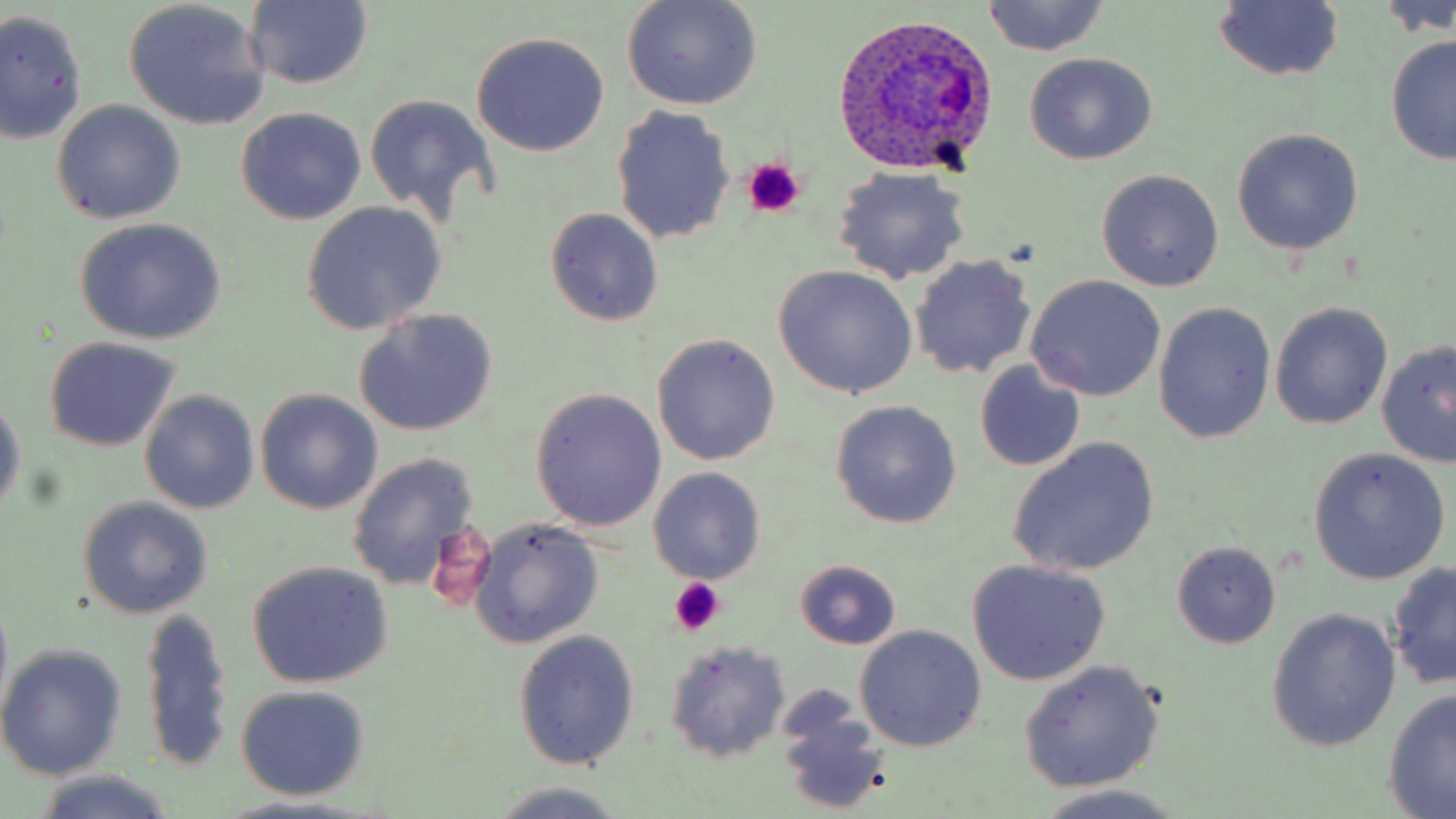 Approximate bounding boxes as named x1/y1/x2/y2 corners in pixels. Plasmodium ovale-infected red blood cell locations: (x1=831, y1=13, x2=998, y2=174). Platelet locations: (x1=742, y1=159, x2=804, y2=219), (x1=668, y1=579, x2=726, y2=636). Uninfected red blood cell locations: (x1=620, y1=0, x2=763, y2=110), (x1=1382, y1=0, x2=1455, y2=38), (x1=246, y1=1, x2=373, y2=89), (x1=1210, y1=1, x2=1345, y2=83), (x1=123, y1=2, x2=270, y2=129), (x1=983, y1=2, x2=1111, y2=56), (x1=1, y1=11, x2=88, y2=145), (x1=473, y1=31, x2=610, y2=156), (x1=1384, y1=35, x2=1456, y2=166), (x1=1024, y1=52, x2=1157, y2=166), (x1=364, y1=93, x2=498, y2=223), (x1=52, y1=101, x2=184, y2=223), (x1=236, y1=107, x2=367, y2=225), (x1=611, y1=107, x2=735, y2=243), (x1=1231, y1=127, x2=1364, y2=255), (x1=832, y1=166, x2=972, y2=285), (x1=1096, y1=169, x2=1224, y2=291), (x1=300, y1=202, x2=447, y2=335), (x1=545, y1=207, x2=665, y2=327), (x1=75, y1=218, x2=226, y2=344), (x1=910, y1=253, x2=1036, y2=380), (x1=773, y1=265, x2=918, y2=399), (x1=1027, y1=275, x2=1167, y2=400), (x1=1153, y1=302, x2=1276, y2=443), (x1=1269, y1=302, x2=1392, y2=430), (x1=353, y1=309, x2=498, y2=436), (x1=652, y1=334, x2=781, y2=466), (x1=45, y1=338, x2=180, y2=452), (x1=1377, y1=340, x2=1456, y2=468), (x1=975, y1=360, x2=1085, y2=473), (x1=255, y1=388, x2=383, y2=514), (x1=529, y1=388, x2=667, y2=532), (x1=140, y1=390, x2=259, y2=513), (x1=0, y1=391, x2=24, y2=518), (x1=831, y1=401, x2=961, y2=528), (x1=1007, y1=438, x2=1159, y2=576), (x1=1307, y1=447, x2=1448, y2=586), (x1=347, y1=453, x2=481, y2=592), (x1=650, y1=468, x2=764, y2=584), (x1=77, y1=497, x2=212, y2=619), (x1=471, y1=519, x2=604, y2=648), (x1=1173, y1=542, x2=1280, y2=649), (x1=966, y1=559, x2=1111, y2=685), (x1=247, y1=560, x2=394, y2=687), (x1=797, y1=560, x2=900, y2=650), (x1=1386, y1=562, x2=1456, y2=691), (x1=140, y1=607, x2=235, y2=776), (x1=1266, y1=608, x2=1400, y2=753), (x1=855, y1=626, x2=986, y2=753), (x1=512, y1=629, x2=640, y2=771), (x1=662, y1=641, x2=790, y2=765), (x1=0, y1=643, x2=128, y2=779), (x1=1018, y1=659, x2=1164, y2=793), (x1=233, y1=686, x2=372, y2=802), (x1=1383, y1=687, x2=1456, y2=816), (x1=773, y1=701, x2=892, y2=817), (x1=30, y1=771, x2=180, y2=819), (x1=483, y1=782, x2=633, y2=819), (x1=1028, y1=788, x2=1190, y2=819). Slide-level diagnosis: Plasmodium ovale. Optical microscopy. Single field of view. Captured at 1000x magnification. May-Grünwald-Giemsa-stained preparation. Image is 1456×819 pixels. Thin blood smear.